State which parasite is depicted.
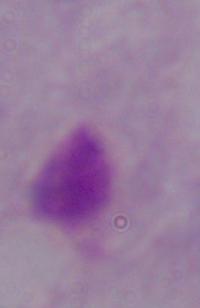

This is a trichomonad.

Micrograph. Captured at 1000x magnification.